Report the malaria status of this cell.
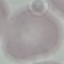
It is uninfected.

Giemsa-stained preparation. Acquired by smartphone through the microscope eyepiece. Thin blood film. Automatically extracted cell patch, resized to 64 × 64 pixels.